Assess the morphology of the red blood cells.
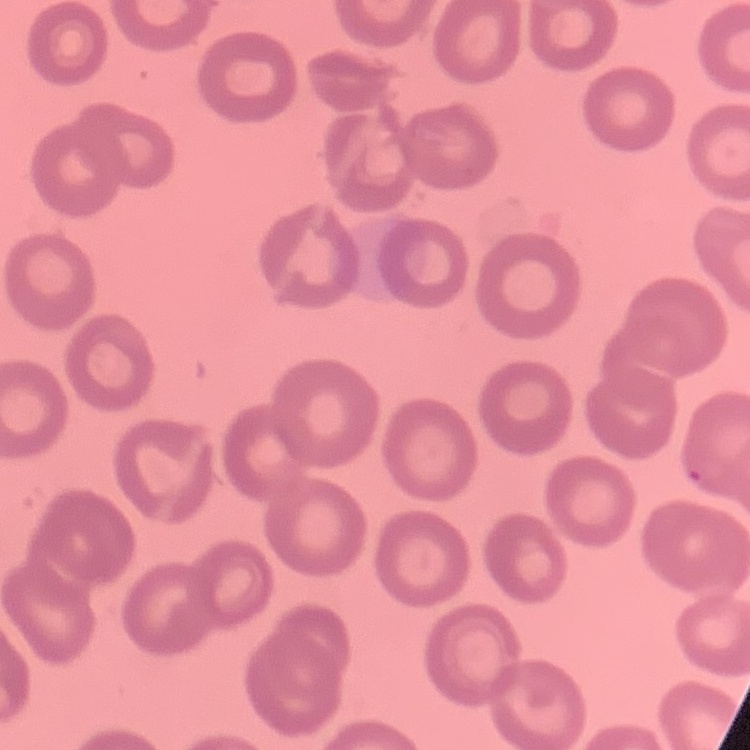

They show no rouleaux formation.

stain = Field's or Giemsa
preparation = thin blood film
image type = one tile cut from a larger photomicrograph